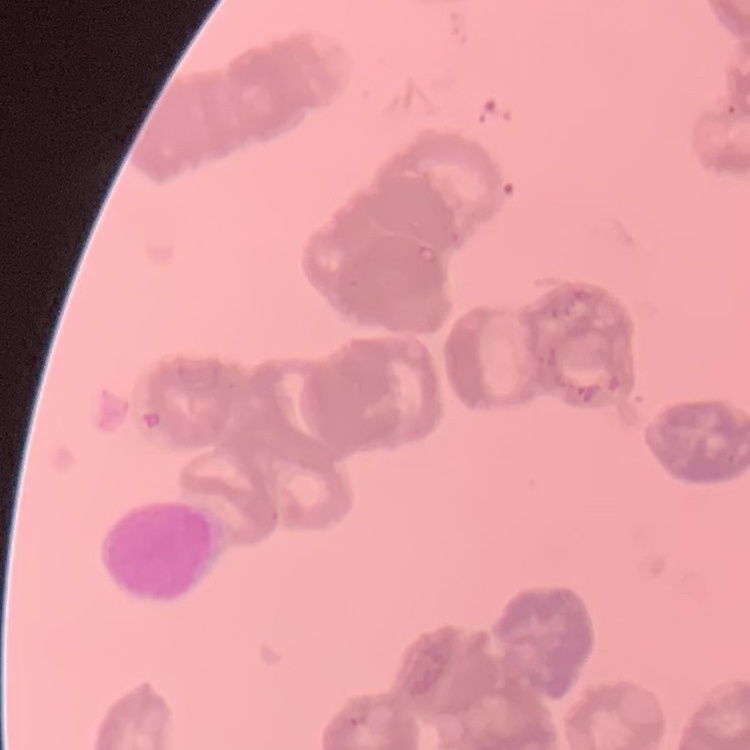

Summary:
  - Red blood cell morphology: rouleaux formation
  - Image type: square crop of a larger photomicrograph
  - Preparation: thin blood film
  - Stain: Field's or Giemsa